Locate every Plasmodium falciparum-infected red blood cell.
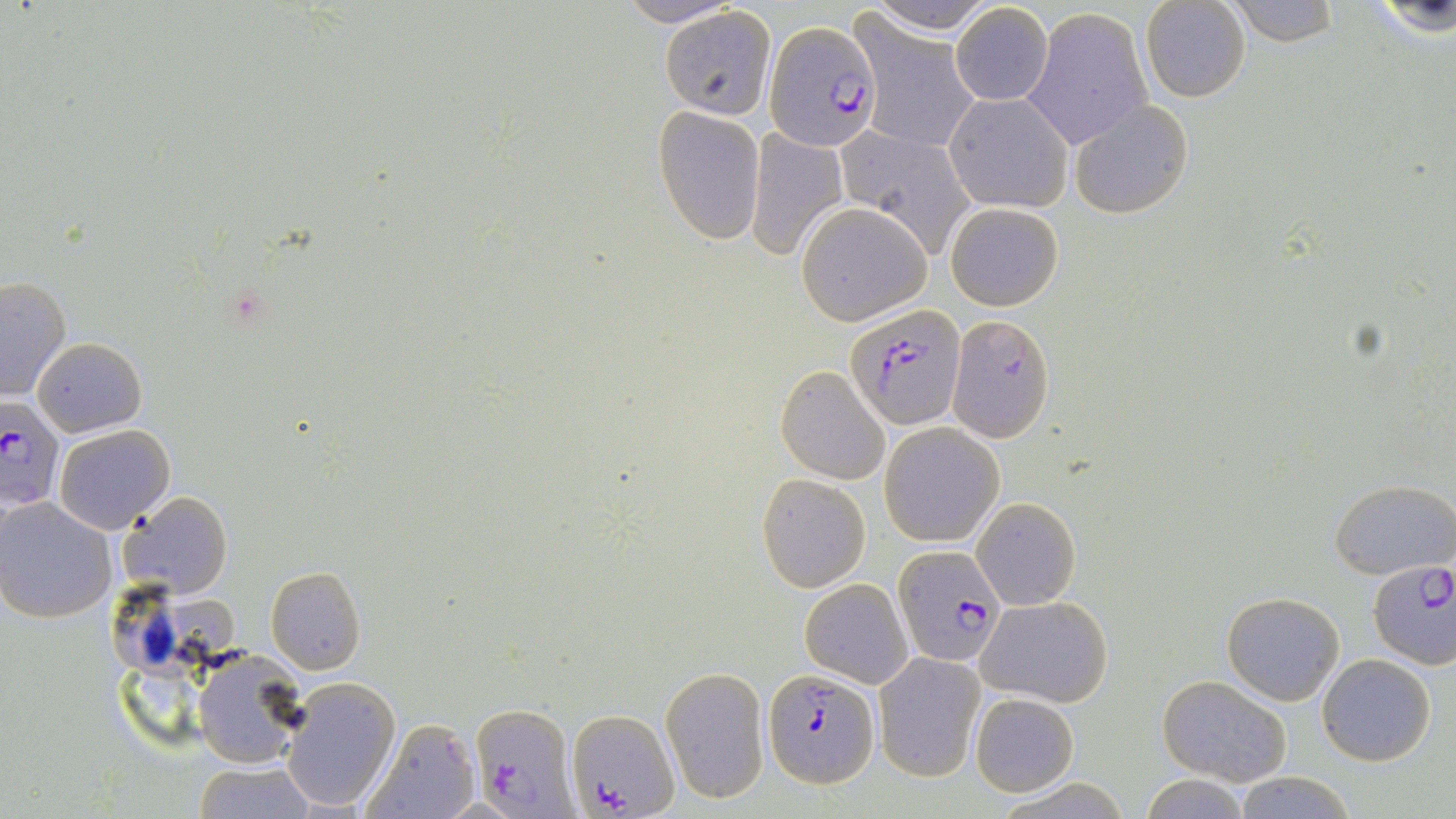

Approximate bounding boxes as (x1, y1, x2, y2) in pixels.
Plasmodium falciparum-infected red blood cells: (765, 22, 880, 151), (846, 302, 963, 430), (947, 315, 1055, 442), (0, 398, 65, 512), (894, 547, 1007, 669), (1366, 556, 1455, 668), (763, 668, 877, 786), (472, 703, 574, 819), (565, 708, 677, 818).

Uninfected red blood cell locations: (613, 0, 745, 27), (864, 0, 996, 36), (1221, 1, 1348, 48), (1359, 1, 1456, 37), (948, 2, 1054, 106), (1140, 2, 1251, 104), (658, 7, 777, 116), (1024, 7, 1152, 149), (853, 15, 980, 150), (943, 92, 1073, 213), (1070, 98, 1192, 218), (653, 105, 765, 244), (833, 125, 975, 254), (745, 128, 850, 261), (795, 201, 933, 325), (945, 201, 1064, 311), (0, 276, 72, 401), (33, 337, 147, 436), (776, 364, 891, 485), (53, 423, 175, 533), (879, 423, 1004, 547), (756, 473, 870, 592), (1330, 478, 1455, 579), (117, 492, 232, 601), (972, 496, 1081, 610), (0, 497, 117, 624), (264, 566, 366, 675), (799, 578, 912, 687), (1220, 591, 1345, 706), (976, 595, 1113, 708), (191, 648, 310, 770), (874, 653, 984, 780), (1316, 654, 1437, 766), (662, 665, 770, 804), (1158, 675, 1293, 785), (280, 677, 401, 813), (968, 692, 1080, 796), (361, 717, 482, 819), (191, 761, 319, 818), (1232, 772, 1359, 819), (1138, 773, 1253, 818). Slide-level diagnosis: Plasmodium falciparum. Thin blood smear. May-Grünwald-Giemsa-stained preparation. Optical microscopy. Single field of view. Image is 1456×819 pixels. 1000x magnification.